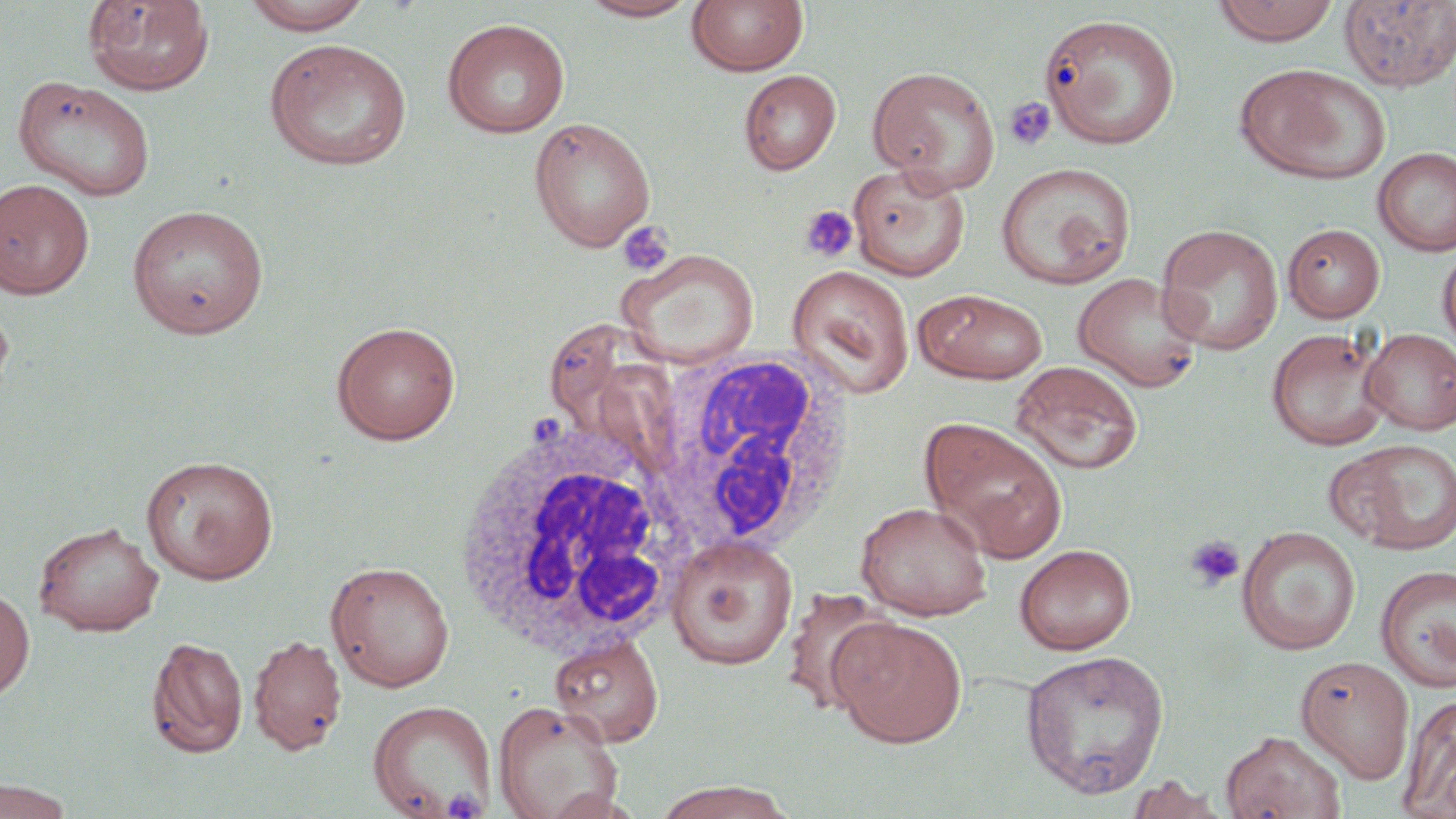 Approximate bounding boxes as [x1, y1, x2, y2] in pixels. Uninfected red blood cell locations: [240, 0, 374, 34], [577, 0, 701, 21], [1211, 0, 1340, 46], [82, 1, 215, 96], [687, 1, 808, 76], [1339, 1, 1456, 92], [1040, 12, 1181, 148], [442, 18, 570, 139], [263, 38, 413, 171], [1236, 63, 1390, 185], [867, 65, 1000, 192], [738, 69, 841, 175], [12, 75, 156, 201], [528, 116, 656, 252], [1372, 146, 1456, 256], [994, 161, 1136, 289], [847, 163, 971, 280], [0, 178, 95, 299], [126, 203, 269, 339], [1155, 223, 1284, 356], [1282, 223, 1386, 322], [1437, 242, 1456, 359], [616, 248, 759, 368], [787, 265, 915, 399], [1072, 271, 1204, 392], [915, 288, 1048, 383], [0, 296, 14, 404], [331, 320, 461, 445], [1266, 327, 1393, 451], [1360, 328, 1456, 435], [1010, 360, 1144, 475], [921, 418, 1068, 562], [1329, 438, 1456, 556], [141, 454, 279, 584], [855, 500, 992, 619], [33, 521, 164, 636], [1236, 526, 1361, 655], [666, 535, 799, 670], [1014, 544, 1136, 655], [325, 560, 454, 692], [1375, 564, 1456, 691], [1, 585, 35, 701], [779, 587, 895, 716], [831, 618, 967, 747], [248, 633, 347, 756], [549, 633, 664, 747], [146, 635, 248, 759], [1020, 649, 1169, 799], [1295, 657, 1415, 783], [1399, 693, 1456, 818], [368, 699, 495, 816], [493, 699, 622, 819], [1220, 729, 1347, 818], [1125, 775, 1225, 819], [0, 777, 77, 819], [651, 782, 798, 818]. White blood cell locations: [650, 347, 857, 559], [454, 420, 687, 660]. Platelet locations: [1004, 96, 1057, 152], [798, 204, 859, 264], [617, 221, 674, 276], [1183, 534, 1246, 592], [443, 788, 487, 818]. Slide-level diagnosis: no evidence of blood parasites. Light microscopy. Image is 1456×819 pixels. 1000x magnification. Thin blood smear. One field of a larger specimen. May-Grünwald-Giemsa stain.